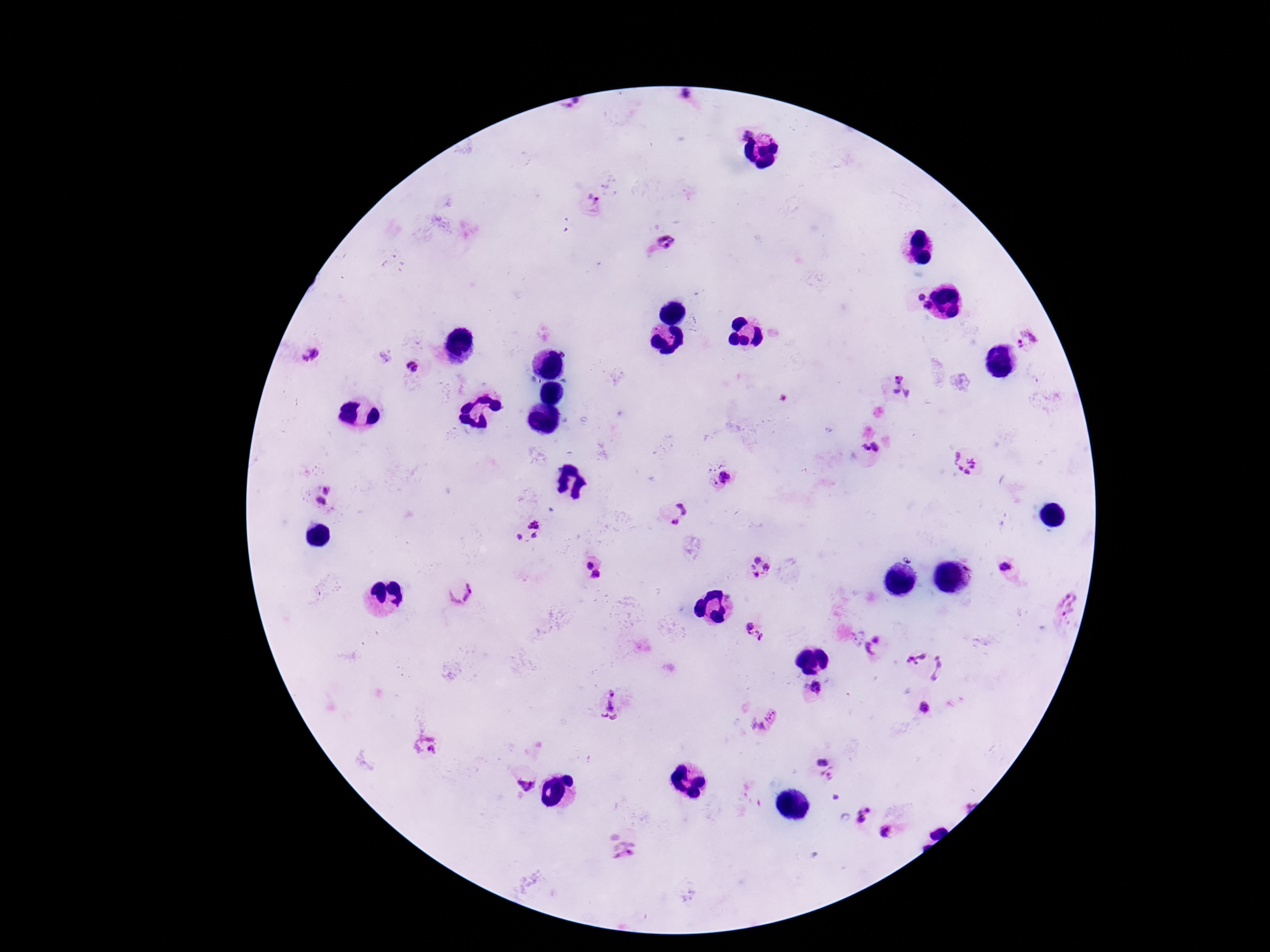 Approximate centers as {x, y} in pixels. Plasmodium parasite locations: {687, 97}, {592, 203}, {666, 241}, {919, 296}, {928, 307}, {1027, 339}, {564, 353}, {309, 354}, {412, 367}, {899, 379}, {896, 392}, {907, 393}, {869, 448}, {965, 464}, {724, 477}, {327, 488}, {319, 503}, {683, 509}, {675, 521}, {535, 522}, {535, 535}, {518, 537}, {757, 559}, {588, 564}, {767, 567}, {753, 568}, {1004, 568}, {756, 574}, {596, 575}, {458, 589}, {1067, 606}, {748, 627}, {759, 634}, {858, 638}, {875, 645}, {917, 657}, {941, 668}, {814, 688}, {614, 705}, {925, 708}, {764, 719}, {427, 746}, {822, 760}, {829, 776}, {526, 784}, {837, 799}, {862, 812}, {894, 829}, {623, 851}. Thick blood film. Smartphone photograph taken through the microscope eyepiece. Patient malaria status: infected. Giemsa-stained preparation. Single field of view. 100x magnification. Image is 1270×952 pixels.